Classify this cell by malaria status.
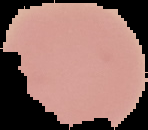
Uninfected.

Segmented cell region on a black background. From a thin blood film. Image is 148×130 pixels.